Describe the morphology of the red blood cells.
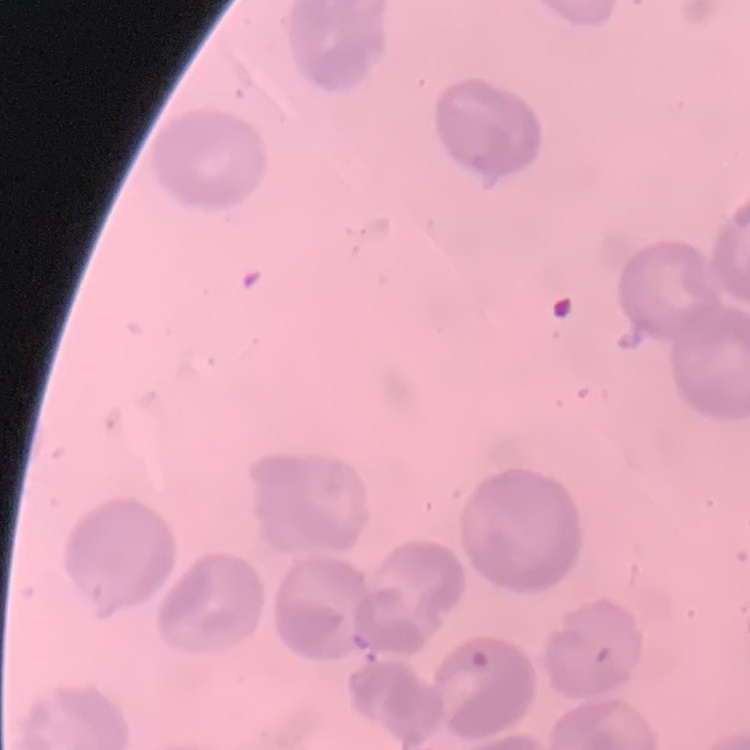
No rouleaux formation.

image_type: one tile cut from a larger photomicrograph
preparation: thin blood smear
stain: Field's or Giemsa